Outline each uninfected red blood cell.
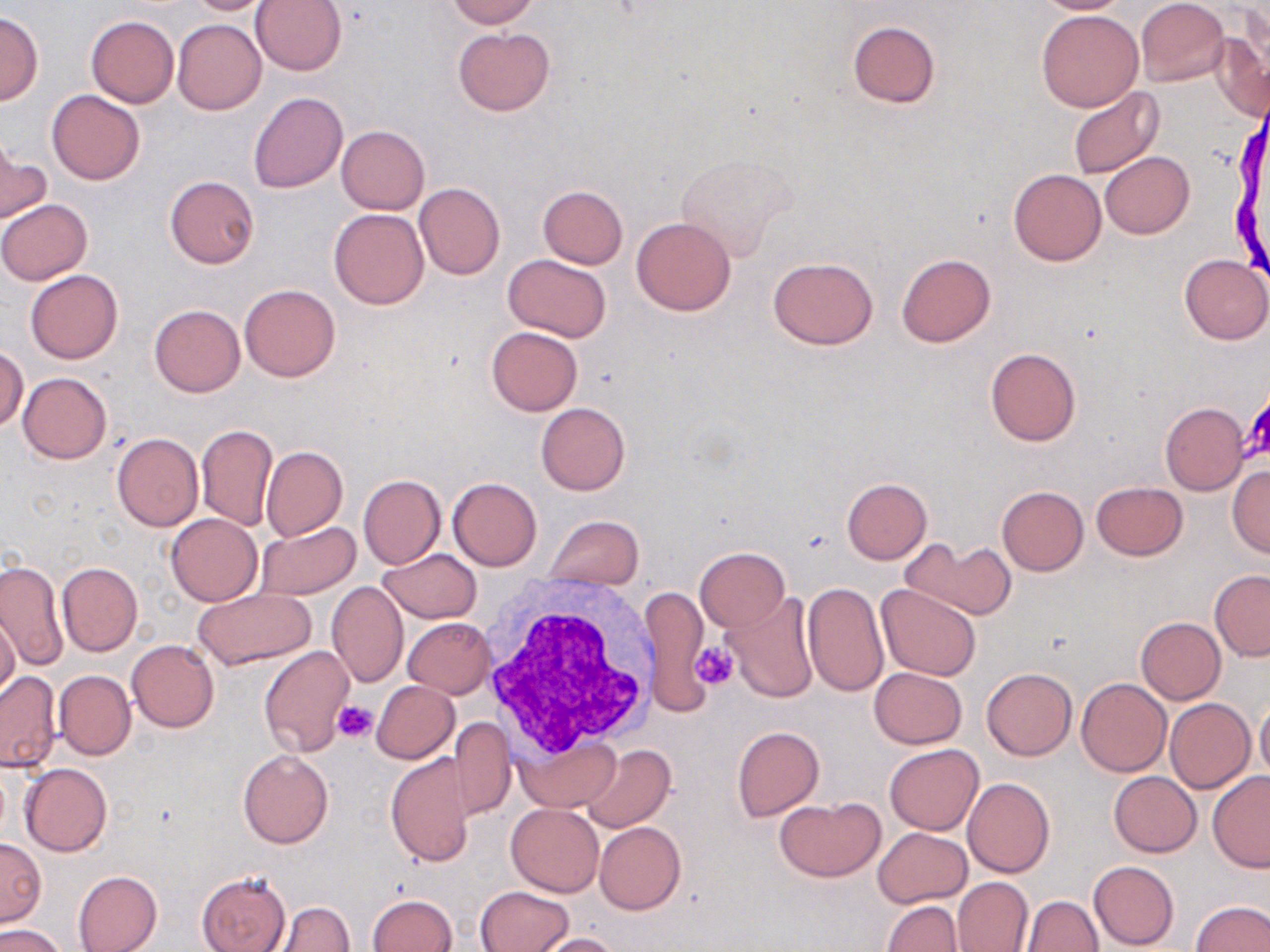
Approximate bounding boxes as [x1, y1, x2, y2] in pixels.
Uninfected red blood cells: [183, 0, 275, 14], [250, 0, 347, 75], [446, 0, 537, 27], [1032, 0, 1132, 14], [1136, 0, 1228, 87], [1036, 8, 1144, 111], [0, 10, 43, 104], [85, 15, 178, 107], [172, 18, 266, 115], [848, 20, 940, 108], [453, 26, 555, 117], [1210, 30, 1270, 122], [1069, 88, 1165, 180], [47, 90, 145, 185], [248, 92, 347, 193], [337, 125, 429, 214], [0, 140, 50, 225], [1100, 151, 1193, 239], [675, 153, 797, 259], [1009, 169, 1106, 265], [165, 176, 260, 268], [414, 182, 506, 280], [538, 185, 628, 269], [0, 199, 91, 284], [328, 208, 429, 310], [632, 216, 736, 315], [896, 253, 996, 347], [504, 254, 611, 342], [1180, 254, 1270, 344], [767, 257, 877, 350], [25, 270, 123, 364], [239, 284, 340, 381], [150, 305, 245, 397], [486, 326, 584, 415], [0, 346, 27, 431], [986, 348, 1081, 446], [18, 371, 112, 464], [536, 401, 631, 496], [1160, 401, 1248, 495], [196, 425, 278, 530], [112, 432, 204, 532], [261, 445, 348, 543], [1226, 465, 1270, 558], [358, 474, 445, 569], [448, 477, 542, 571], [842, 477, 932, 564], [1092, 480, 1187, 560], [997, 486, 1087, 574], [166, 514, 263, 605], [545, 515, 643, 588], [253, 521, 362, 599], [905, 538, 1016, 620], [695, 547, 789, 631], [378, 549, 482, 623], [0, 558, 66, 671], [57, 562, 142, 655], [1210, 570, 1270, 660], [327, 581, 408, 688], [802, 582, 888, 696], [876, 584, 981, 679], [641, 585, 712, 716], [191, 587, 319, 671], [722, 593, 819, 702], [0, 615, 20, 699], [402, 617, 496, 698], [1135, 617, 1225, 704], [126, 639, 218, 733], [259, 645, 354, 757], [869, 667, 968, 749], [982, 667, 1077, 760], [0, 670, 60, 772], [54, 670, 135, 759], [1075, 677, 1171, 776], [372, 680, 459, 763], [1165, 697, 1254, 792], [1255, 701, 1270, 782], [449, 716, 514, 820], [732, 726, 825, 821], [513, 735, 618, 812], [885, 743, 982, 835], [580, 744, 677, 832], [238, 749, 334, 848], [385, 754, 474, 867], [20, 763, 111, 856], [1108, 771, 1201, 857], [1207, 772, 1270, 872], [962, 778, 1055, 879], [775, 796, 887, 880], [505, 804, 604, 896], [594, 822, 685, 914], [873, 827, 972, 908], [0, 839, 46, 925], [1088, 860, 1179, 950], [72, 869, 162, 952], [197, 871, 290, 952], [952, 876, 1033, 952], [476, 885, 573, 952], [368, 893, 457, 952], [1023, 895, 1103, 951], [881, 900, 964, 951], [1192, 900, 1270, 951], [275, 901, 355, 951], [0, 925, 66, 952], [533, 932, 624, 952].

slide-level diagnosis = negative for blood parasites
preparation = thin blood film
modality = optical microscopy
field of view = one of a larger specimen
image size = 1270×952 pixels
magnification = 1000x
white blood cell locations = approximate bounding boxes as [x1, y1, x2, y2] in pixels: [479, 576, 661, 767]
platelet locations = approximate bounding boxes as [x1, y1, x2, y2] in pixels: [1244, 394, 1270, 465], [692, 641, 735, 689], [333, 701, 379, 743]
stain = May-Grünwald-Giemsa